Report the malaria status of this cell.
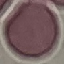

It is uninfected.

Summary:
  - Image type: automatically extracted cell patch, resized to 64 × 64 pixels
  - Capture: smartphone through the microscope eyepiece
  - Preparation: thin blood film
  - Stain: Giemsa